Locate every leukocyte (white blood cell).
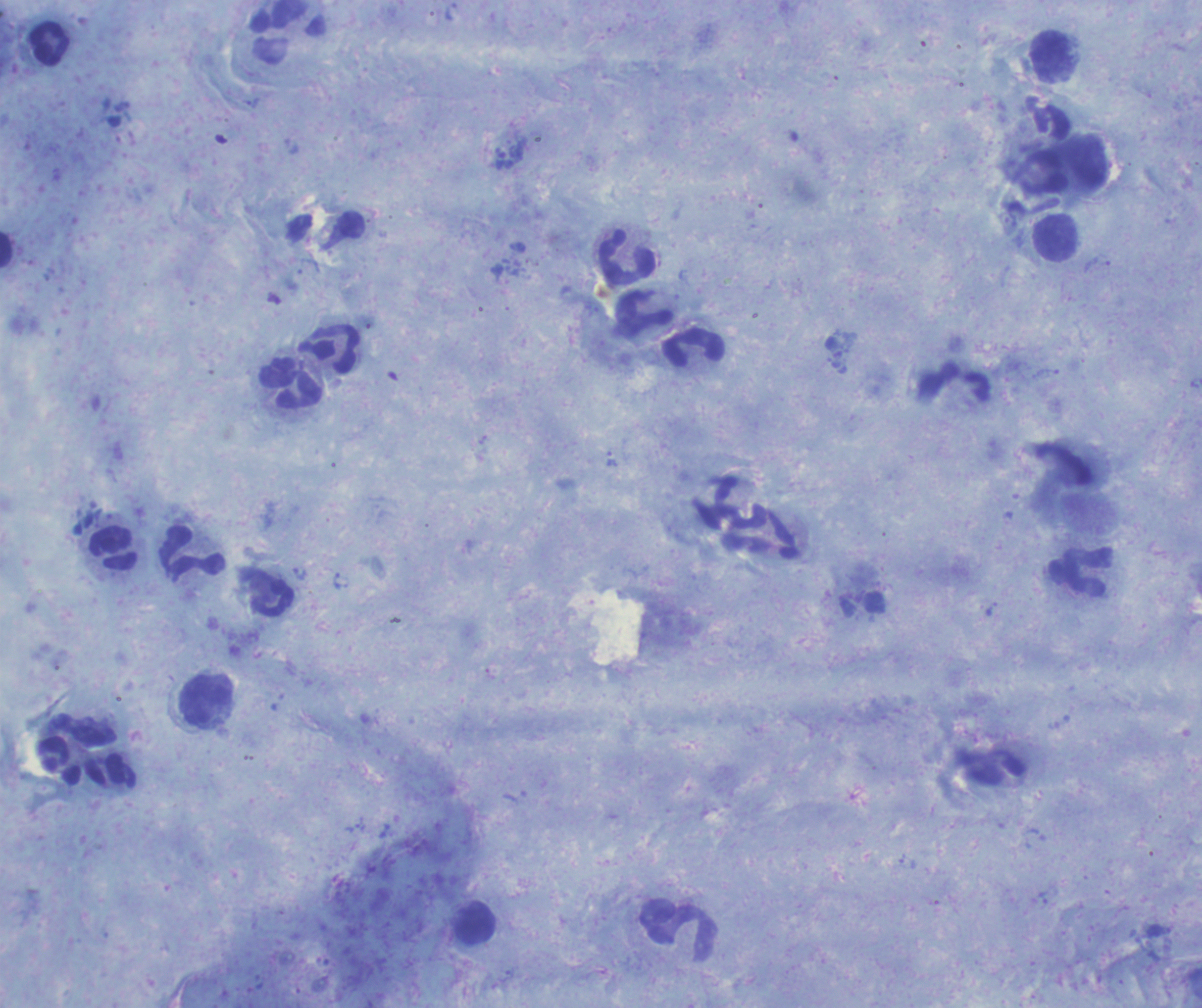
Approximate object centers, in pixels from the top-left corner.
Leukocytes: (x=288, y=34), (x=48, y=44), (x=1051, y=56), (x=1055, y=238), (x=627, y=259), (x=642, y=314), (x=329, y=348), (x=694, y=348), (x=290, y=384), (x=954, y=385), (x=733, y=503), (x=114, y=549), (x=192, y=555), (x=1081, y=574), (x=207, y=699), (x=475, y=925), (x=679, y=932).

stain: Romanowsky
field_of_view: single
preparation: thick blood smear
magnification: 100x
trophozoite_locations: 'approximate object centers, in pixels from the top-left corner: (x=612, y=460), (x=299, y=573)'
image_size: 1202×1008 pixels
result: positive for Plasmodium parasites
background_quality: good
context: previously used in a real diagnosis
coloration_quality: good